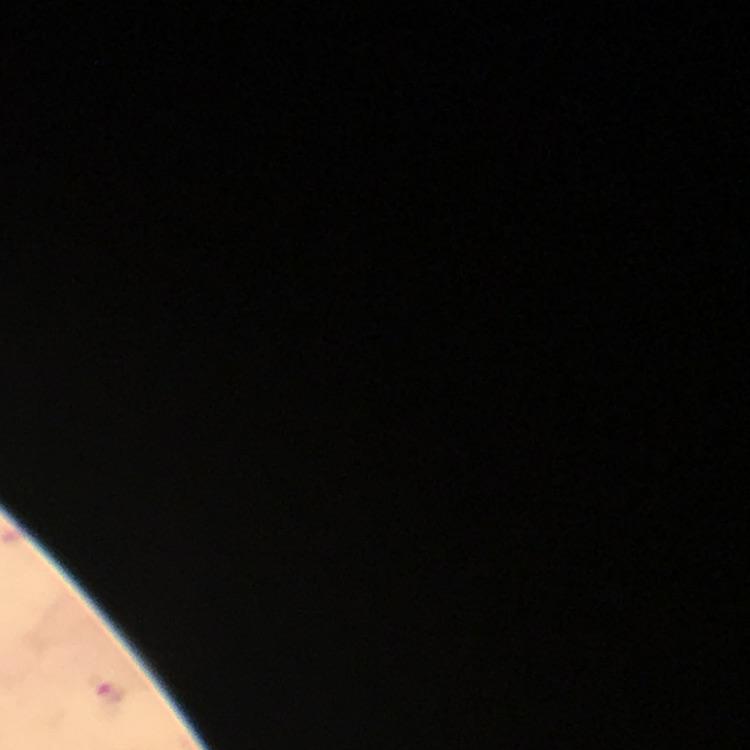

Approximate centers as {x, y} in pixels.
Summary:
  - Plasmodium parasite locations: {106, 696}
  - Stain: Giemsa
  - Image size: 750×750 pixels
  - Preparation: thick blood film
  - Capture: smartphone photograph through a microscope
  - Immersion oil: used
  - Cropped from: a single field of view
  - Context: from a diagnostic examination for malaria
  - Magnification: 100x